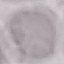
Result: negative for malaria parasites. Acquired by smartphone through the microscope eyepiece. Thin blood film. Giemsa-stained preparation. Automatically extracted cell patch, resized to 64 × 64 pixels.